Outline each Babesia divergens-infected red blood cell.
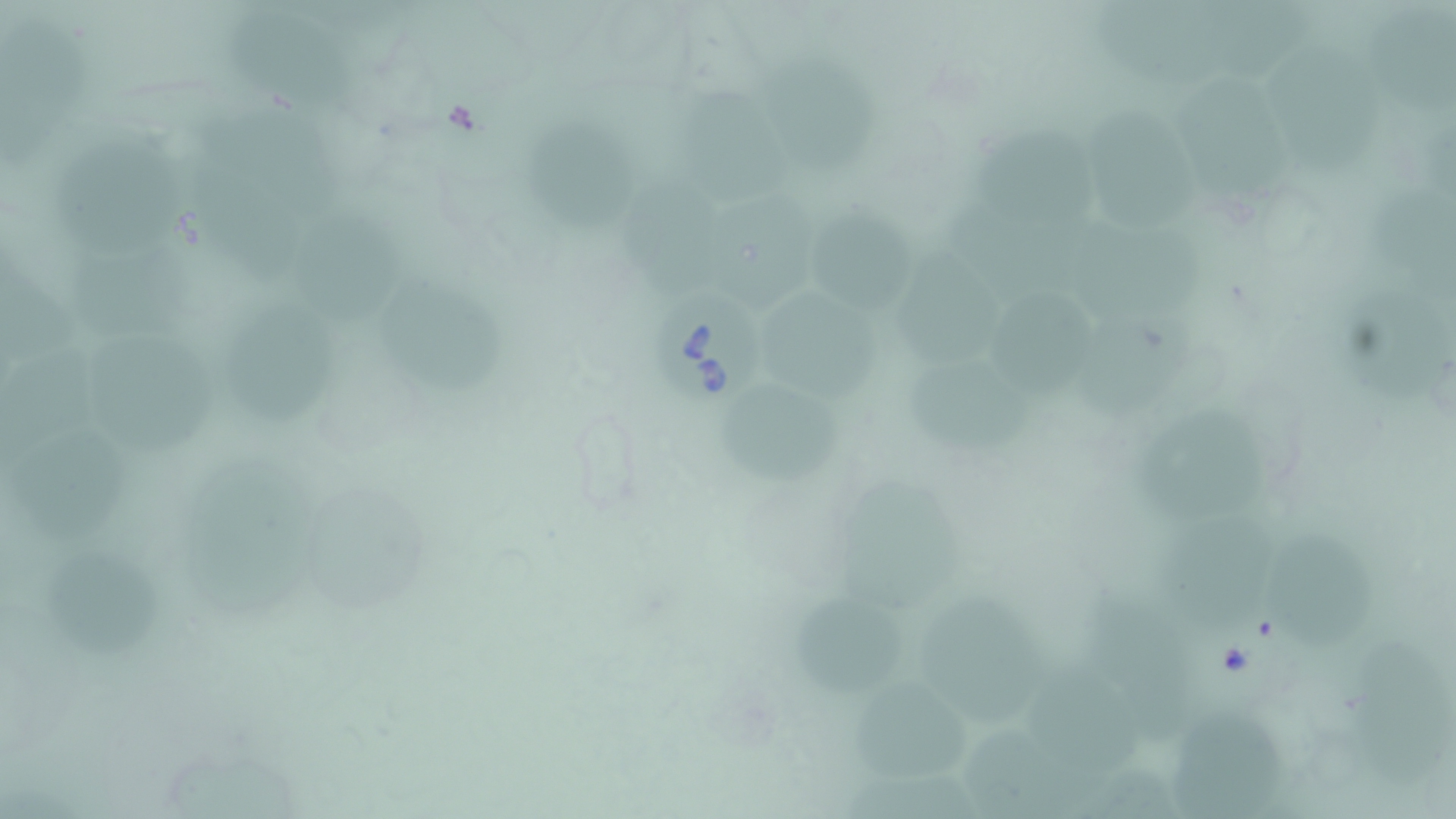

Approximate bounding boxes as named x1/y1/x2/y2 corners in pixels.
Babesia divergens-infected red blood cells: (x1=649, y1=289, x2=765, y2=415).

slide-level diagnosis = Babesia divergens
uninfected red blood cell locations = approximate bounding boxes as named x1/y1/x2/y2 corners in pixels: (x1=1095, y1=0, x2=1229, y2=72), (x1=1369, y1=5, x2=1456, y2=117), (x1=1223, y1=7, x2=1310, y2=86), (x1=4, y1=11, x2=94, y2=161), (x1=228, y1=15, x2=361, y2=117), (x1=1268, y1=45, x2=1388, y2=180), (x1=759, y1=58, x2=879, y2=164), (x1=1173, y1=73, x2=1286, y2=203), (x1=681, y1=89, x2=787, y2=203), (x1=1090, y1=98, x2=1192, y2=230), (x1=197, y1=102, x2=355, y2=218), (x1=532, y1=120, x2=637, y2=242), (x1=993, y1=129, x2=1110, y2=238), (x1=56, y1=148, x2=189, y2=254), (x1=189, y1=164, x2=306, y2=283), (x1=626, y1=164, x2=728, y2=297), (x1=945, y1=178, x2=1058, y2=293), (x1=1370, y1=178, x2=1455, y2=285), (x1=727, y1=187, x2=815, y2=306), (x1=291, y1=200, x2=410, y2=322), (x1=822, y1=212, x2=916, y2=313), (x1=1078, y1=216, x2=1219, y2=328), (x1=78, y1=243, x2=208, y2=332), (x1=4, y1=251, x2=78, y2=369), (x1=902, y1=253, x2=1019, y2=368), (x1=1337, y1=273, x2=1451, y2=406), (x1=385, y1=278, x2=519, y2=407), (x1=767, y1=289, x2=881, y2=410), (x1=996, y1=293, x2=1099, y2=393), (x1=240, y1=299, x2=347, y2=428), (x1=1086, y1=316, x2=1196, y2=422), (x1=91, y1=326, x2=218, y2=455), (x1=0, y1=340, x2=98, y2=470), (x1=913, y1=360, x2=1054, y2=455), (x1=721, y1=381, x2=846, y2=489), (x1=1140, y1=403, x2=1272, y2=523), (x1=12, y1=419, x2=130, y2=542), (x1=189, y1=460, x2=323, y2=623), (x1=845, y1=478, x2=961, y2=613), (x1=324, y1=491, x2=438, y2=617), (x1=1168, y1=511, x2=1282, y2=624), (x1=1282, y1=537, x2=1385, y2=652), (x1=32, y1=549, x2=164, y2=658), (x1=921, y1=578, x2=1047, y2=714), (x1=1085, y1=585, x2=1193, y2=733), (x1=787, y1=593, x2=902, y2=695), (x1=1351, y1=637, x2=1456, y2=786), (x1=1036, y1=649, x2=1141, y2=785), (x1=854, y1=678, x2=973, y2=774), (x1=1176, y1=702, x2=1278, y2=814), (x1=959, y1=722, x2=1077, y2=814), (x1=166, y1=737, x2=307, y2=817), (x1=1082, y1=746, x2=1177, y2=817), (x1=824, y1=757, x2=973, y2=816)
image size = 1456×819 pixels
magnification = 1000x
preparation = thin blood smear
stain = May-Grünwald-Giemsa
field of view = one of a larger specimen
modality = optical microscopy